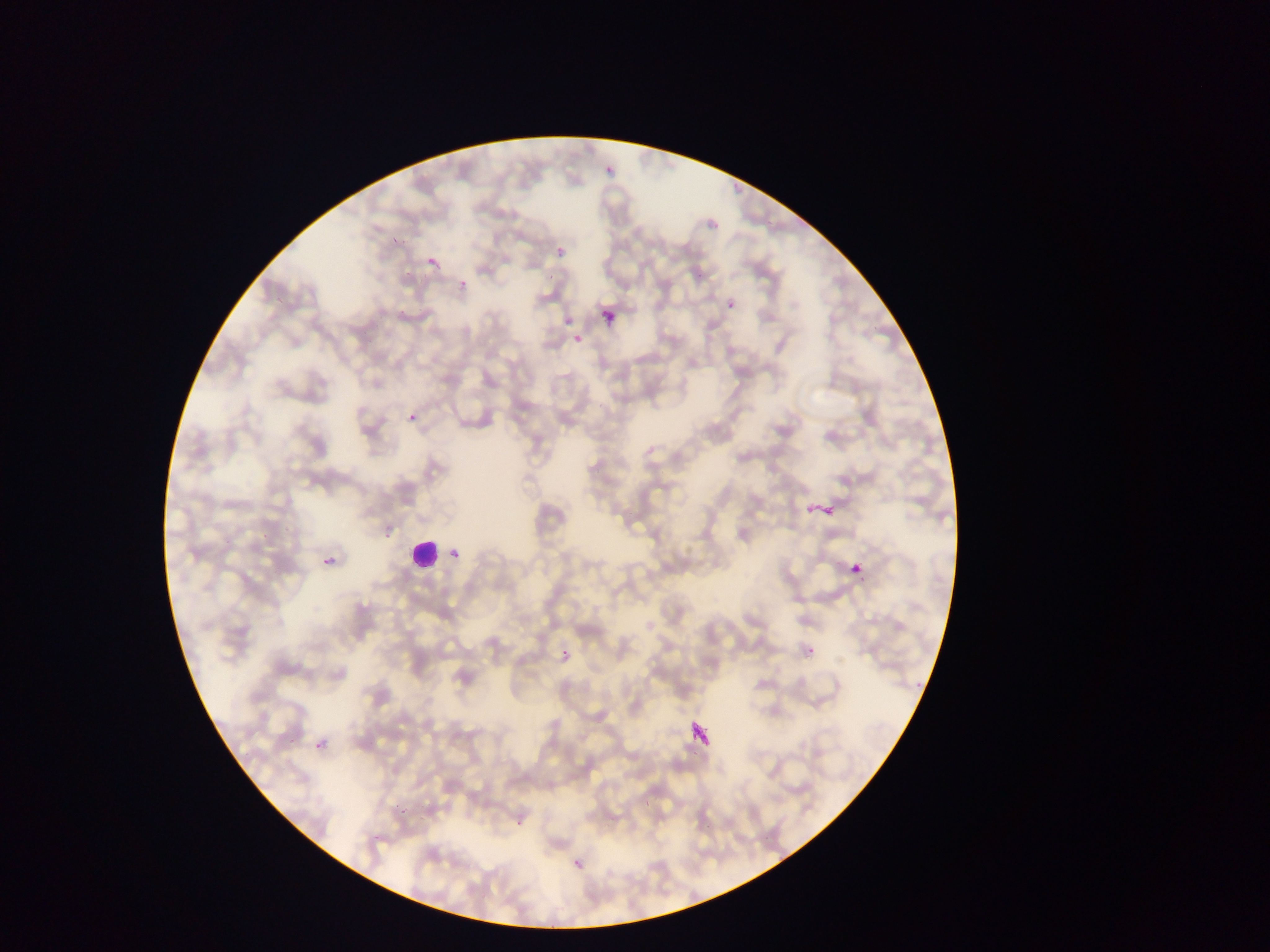

Approximate bounding boxes as (left, top, right, bottom) in pixels. Plasmodium parasite locations: (604, 163, 617, 177), (553, 246, 568, 262), (421, 249, 449, 268), (725, 299, 737, 313), (602, 309, 617, 325), (573, 334, 585, 346), (402, 408, 420, 420), (807, 498, 839, 526), (447, 546, 463, 564), (320, 553, 340, 575), (845, 556, 868, 582), (801, 636, 822, 668), (557, 646, 574, 666), (696, 704, 718, 756), (314, 737, 331, 758), (569, 855, 588, 875). Leukocyte locations: (404, 536, 442, 573). Image is 1270×952 pixels. Mobile-phone photograph taken through the microscope. Sample from Ghana. Thin blood smear. Single field of view.